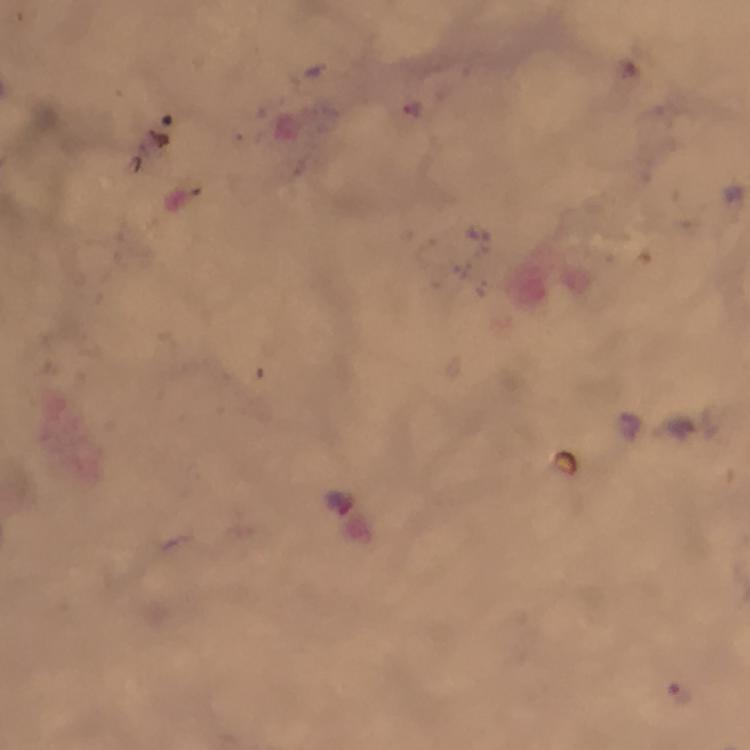
{
  "image_size": "750×750 pixels",
  "capture": "smartphone photograph through a microscope",
  "preparation": "thick blood smear",
  "magnification": "100x",
  "context": "from a diagnostic examination for malaria",
  "cropped_from": "one field of view",
  "stain": "Giemsa",
  "malaria_parasite_locations": "approximate object centers, in pixels from the top-left corner: (x=678, y=693)",
  "immersion_oil": "applied"
}